Identify the parasite.
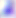

This is Toxoplasma gondii.

magnification = 400x
modality = micrograph